Outline each Plasmodium falciparum-infected red blood cell.
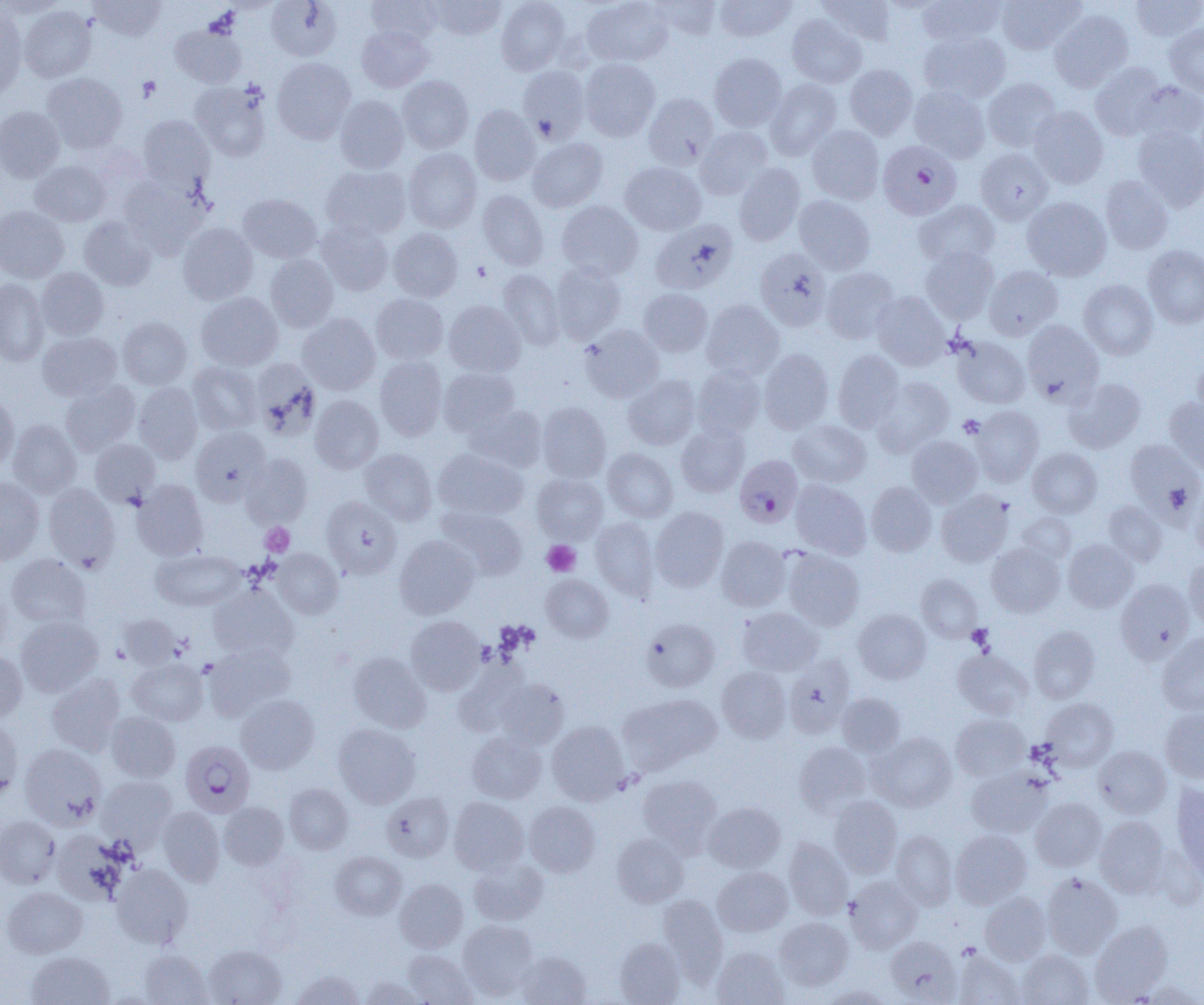

Approximate bounding boxes as (x1, y1, x2, y2) in pixels.
Plasmodium falciparum-infected red blood cells: (878, 140, 962, 220), (734, 455, 803, 527), (181, 741, 255, 817).

Platelet locations: (472, 262, 491, 281), (958, 415, 985, 438), (260, 522, 294, 556), (542, 540, 580, 576), (967, 624, 994, 652). Uninfected red blood cell locations: (1, 0, 64, 18), (88, 0, 166, 40), (266, 0, 342, 61), (366, 0, 442, 44), (430, 0, 506, 40), (496, 0, 570, 75), (581, 0, 674, 67), (650, 0, 722, 39), (715, 0, 796, 42), (818, 0, 896, 45), (917, 0, 1005, 46), (996, 0, 1083, 54), (1130, 0, 1204, 43), (19, 6, 96, 82), (0, 7, 26, 101), (1049, 10, 1133, 91), (787, 13, 866, 87), (170, 24, 246, 88), (1164, 24, 1204, 96), (357, 25, 434, 92), (919, 30, 1011, 103), (709, 52, 787, 131), (272, 58, 356, 144), (579, 58, 660, 141), (1090, 62, 1168, 140), (844, 64, 918, 139), (518, 66, 590, 142), (42, 73, 127, 153), (398, 75, 473, 154), (982, 77, 1060, 152), (764, 79, 841, 159), (190, 81, 271, 161), (1132, 81, 1204, 143), (909, 85, 991, 162), (643, 93, 719, 169), (334, 95, 409, 174), (469, 105, 540, 186), (1029, 105, 1108, 188), (0, 106, 65, 182), (138, 115, 213, 191), (807, 125, 884, 204), (1133, 125, 1204, 211), (696, 126, 772, 198), (527, 137, 607, 211), (403, 147, 482, 232), (976, 148, 1053, 224), (30, 161, 110, 226), (620, 162, 706, 234), (734, 163, 805, 245), (321, 165, 410, 239), (1100, 176, 1173, 254), (120, 177, 208, 256), (477, 190, 548, 270), (238, 194, 321, 263), (793, 195, 875, 274), (1022, 197, 1112, 281), (914, 200, 999, 268), (557, 201, 643, 280), (0, 206, 69, 283), (79, 217, 156, 290), (651, 219, 739, 294), (316, 221, 393, 295), (178, 223, 258, 305), (388, 228, 462, 302), (1143, 245, 1204, 328), (920, 246, 999, 323), (755, 249, 832, 331), (265, 254, 338, 332), (549, 262, 626, 344), (984, 266, 1063, 340), (820, 267, 899, 343), (37, 268, 108, 339), (497, 269, 564, 349), (0, 278, 49, 366), (1078, 280, 1158, 359), (638, 288, 712, 357), (871, 291, 951, 370), (196, 292, 283, 371), (371, 294, 448, 364), (444, 300, 525, 377), (701, 300, 785, 380), (297, 313, 380, 395), (118, 317, 192, 389), (1023, 320, 1104, 404), (580, 325, 665, 402), (37, 332, 122, 401), (952, 336, 1030, 408), (759, 349, 833, 433), (833, 349, 904, 432), (375, 355, 447, 440), (1193, 356, 1204, 422), (251, 360, 321, 439), (188, 362, 263, 434), (692, 365, 766, 440), (439, 367, 520, 437), (623, 375, 700, 449), (874, 377, 954, 456), (1064, 378, 1145, 452), (61, 381, 140, 456), (134, 382, 202, 463), (0, 395, 18, 473), (310, 395, 383, 473), (1164, 398, 1204, 473), (537, 402, 611, 483), (466, 404, 547, 472), (971, 405, 1044, 486), (789, 419, 871, 486), (8, 420, 81, 498), (676, 424, 749, 497), (191, 427, 270, 505), (907, 435, 982, 507), (1125, 438, 1202, 517), (90, 439, 160, 507), (1027, 447, 1102, 517), (433, 448, 528, 520), (603, 448, 678, 522), (360, 449, 437, 524), (241, 453, 312, 528), (532, 474, 607, 544), (0, 478, 44, 564), (132, 479, 208, 560), (791, 480, 871, 559), (866, 482, 936, 556), (43, 483, 120, 570), (1191, 486, 1204, 560), (937, 489, 1013, 566), (322, 496, 402, 578), (1103, 501, 1167, 566), (438, 506, 527, 580), (650, 506, 729, 592), (1018, 512, 1076, 564), (591, 517, 659, 602), (395, 535, 479, 618), (716, 536, 791, 611), (1063, 539, 1138, 612), (986, 543, 1064, 617), (273, 549, 343, 618), (784, 549, 864, 630), (152, 550, 245, 611), (7, 554, 91, 629), (1184, 558, 1204, 627), (916, 574, 982, 641), (541, 575, 613, 642), (1116, 579, 1194, 663), (0, 582, 11, 659), (209, 585, 298, 661), (737, 607, 823, 675), (853, 609, 931, 683), (117, 614, 181, 669), (16, 616, 103, 697), (406, 616, 485, 695), (641, 617, 720, 692), (1029, 626, 1100, 703), (1157, 632, 1204, 715), (205, 642, 295, 720), (953, 649, 1034, 719), (0, 650, 27, 723), (348, 652, 430, 732), (783, 656, 855, 738), (128, 657, 207, 725), (716, 666, 791, 742), (46, 673, 125, 756), (493, 678, 569, 749), (619, 693, 721, 774), (837, 693, 905, 757), (236, 694, 318, 773), (1041, 697, 1118, 772), (1160, 707, 1204, 783), (106, 711, 180, 782), (951, 714, 1029, 781), (0, 716, 23, 802), (546, 721, 629, 805), (333, 723, 420, 808), (467, 732, 546, 803), (869, 732, 957, 812), (794, 742, 872, 816), (20, 744, 107, 830), (1094, 746, 1171, 817), (967, 768, 1053, 838), (637, 775, 721, 851), (96, 776, 178, 849), (1171, 782, 1204, 883), (285, 784, 353, 854), (381, 792, 454, 862), (829, 796, 902, 877), (449, 797, 529, 875), (1030, 798, 1106, 871), (524, 801, 601, 876), (220, 802, 289, 869), (703, 802, 785, 872), (157, 807, 225, 886), (0, 816, 60, 888), (1094, 816, 1169, 898), (50, 829, 129, 905), (951, 829, 1031, 908), (891, 830, 957, 910), (612, 833, 688, 907), (784, 838, 852, 920), (330, 851, 406, 920), (469, 858, 548, 925), (112, 864, 193, 948), (713, 867, 793, 936), (1041, 872, 1122, 958), (845, 876, 921, 953), (395, 879, 468, 952), (2, 886, 86, 957), (980, 892, 1050, 964), (658, 894, 727, 982), (775, 917, 854, 990), (458, 919, 538, 1000), (1090, 921, 1173, 1002), (885, 936, 962, 1004), (615, 937, 685, 1004), (205, 944, 286, 1005), (711, 947, 789, 1005), (139, 949, 212, 1004), (1017, 949, 1094, 1005), (403, 950, 477, 1005), (952, 950, 1025, 1005), (27, 951, 113, 1005), (514, 951, 591, 1005), (291, 970, 365, 1004), (359, 977, 424, 1005), (1134, 979, 1204, 1005), (822, 986, 892, 1004). Slide-level diagnosis: Plasmodium falciparum. Single field of view. Image is 1204×1005 pixels. 1000x magnification. Optical microscopy. Thin blood smear.